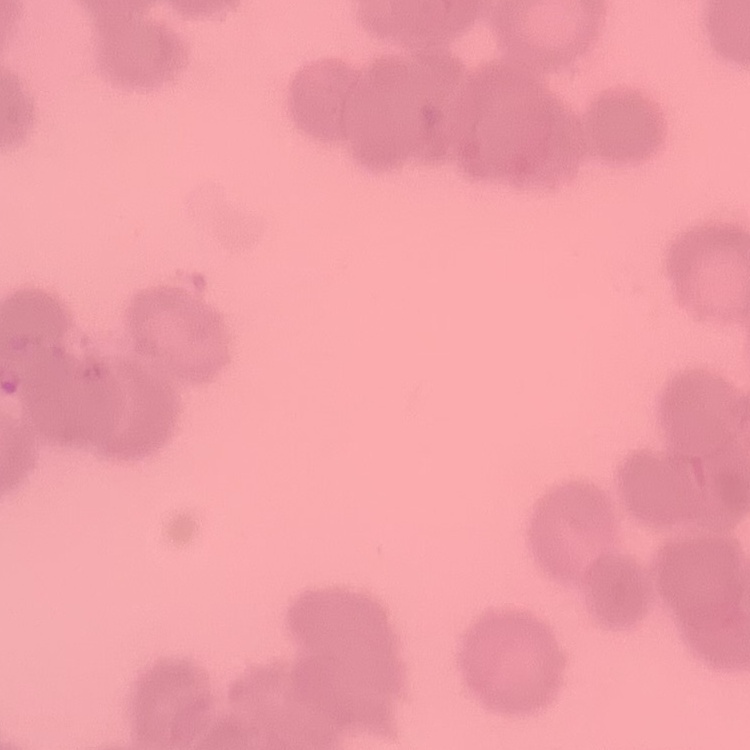

Summary:
  - Red blood cell morphology: rouleaux formation
  - Preparation: thin blood film
  - Stain: Field's or Giemsa
  - Image type: one tile cut from a larger photomicrograph